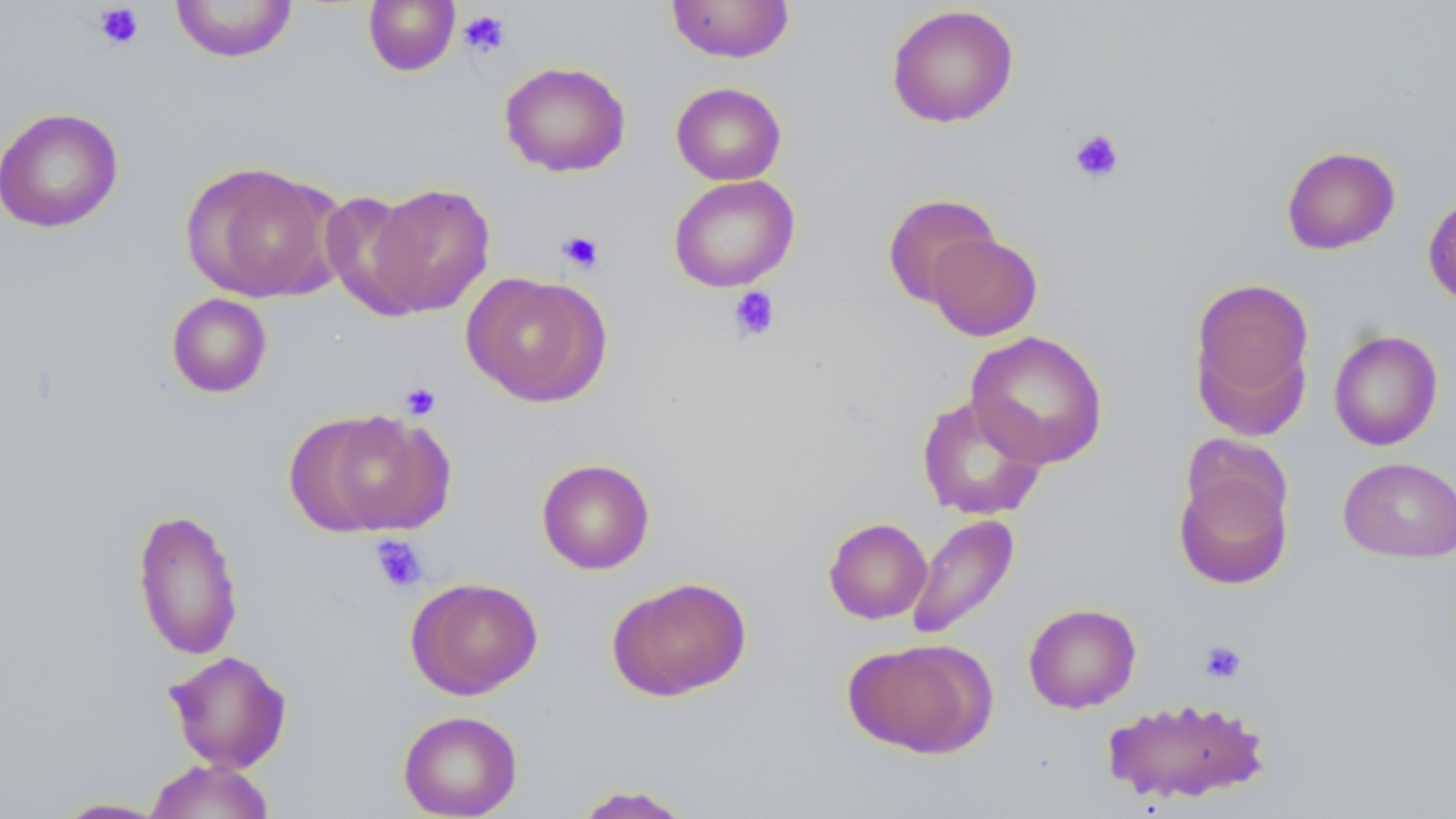
slide-level diagnosis = negative for blood parasites
field of view = one of a larger specimen
uninfected red blood cell locations = approximate bounding boxes as (x1, y1, x2, y2) in pixels: (169, 0, 298, 63), (363, 0, 460, 76), (666, 0, 795, 63), (886, 4, 1019, 128), (499, 61, 631, 178), (671, 81, 787, 185), (0, 107, 124, 233), (1281, 146, 1401, 254), (180, 160, 343, 304), (668, 174, 800, 293), (364, 182, 495, 317), (320, 191, 429, 316), (1423, 191, 1456, 309), (881, 193, 1000, 307), (927, 233, 1043, 341), (462, 272, 612, 407), (1189, 277, 1315, 431), (166, 293, 272, 398), (965, 330, 1108, 469), (1328, 330, 1443, 451), (916, 394, 1048, 521), (292, 409, 454, 537), (1338, 456, 1456, 562), (536, 458, 656, 575), (1173, 463, 1293, 590), (131, 506, 244, 661), (905, 513, 1020, 641), (823, 517, 932, 624), (607, 575, 753, 702), (405, 577, 544, 700), (1023, 603, 1141, 714), (844, 638, 996, 759), (164, 649, 293, 773), (1100, 696, 1273, 806), (397, 710, 523, 818), (143, 758, 276, 818), (571, 784, 695, 818), (48, 797, 173, 818)
image size = 1456×819 pixels
magnification = 1000x
modality = light microscopy
stain = May-Grünwald-Giemsa
platelet locations = approximate bounding boxes as (x1, y1, x2, y2) in pixels: (93, 3, 145, 50), (459, 9, 511, 57), (1069, 128, 1125, 184), (556, 230, 605, 274), (727, 287, 781, 343), (400, 382, 441, 420), (371, 535, 428, 593), (1199, 640, 1247, 684)
preparation = thin blood smear